Identify the parasite.
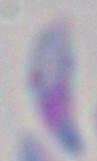
Toxoplasma gondii.

Summary:
  - Magnification: 1000x
  - Modality: micrograph